Locate every blood parasite and identify its species.
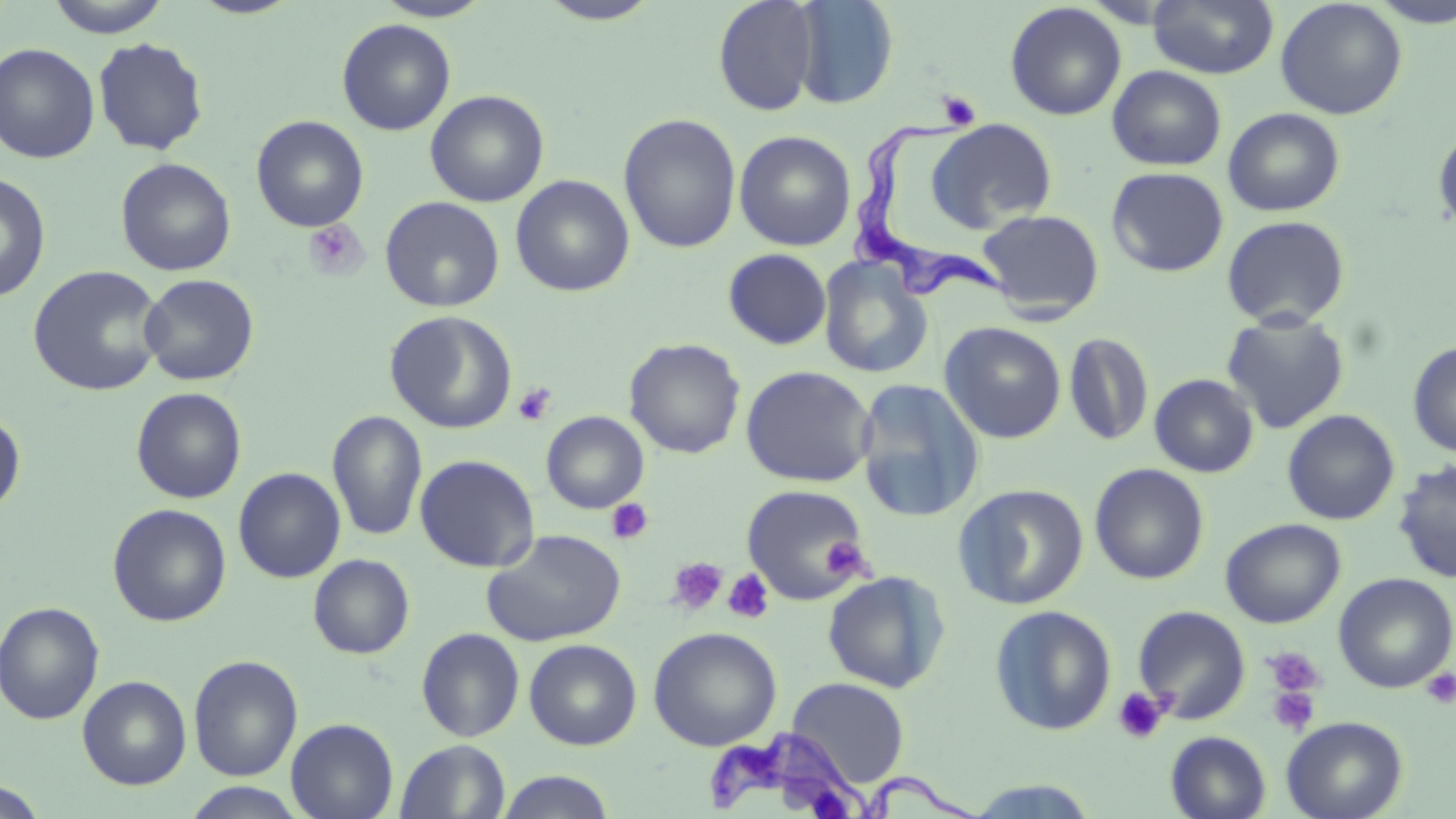
Approximate bounding boxes as [x1, y1, x2, y2] in pixels.
Trypanosoma brucei: [854, 116, 1014, 306], [707, 726, 970, 818].
No Plasmodium falciparum, Plasmodium ovale, Plasmodium malariae, Plasmodium vivax, or Babesia divergens observed.

Summary:
  - Uninfected red blood cell locations: [45, 0, 171, 37], [188, 0, 304, 19], [374, 0, 494, 21], [535, 0, 664, 25], [712, 0, 821, 115], [792, 0, 898, 110], [1147, 0, 1279, 79], [1275, 0, 1408, 120], [1368, 0, 1456, 28], [1005, 2, 1127, 121], [337, 18, 456, 135], [93, 37, 209, 156], [0, 42, 100, 163], [1107, 65, 1226, 171], [425, 90, 549, 207], [1223, 107, 1346, 216], [618, 113, 742, 253], [251, 115, 370, 232], [927, 118, 1057, 233], [1433, 126, 1456, 235], [734, 130, 857, 251], [116, 157, 236, 276], [1107, 167, 1228, 277], [0, 171, 51, 303], [511, 175, 634, 297], [379, 196, 505, 312], [977, 209, 1105, 319], [1222, 215, 1350, 328], [722, 248, 831, 350], [818, 255, 934, 379], [28, 264, 166, 397], [138, 273, 259, 386], [385, 310, 517, 433], [1220, 311, 1350, 434], [940, 321, 1067, 444], [1063, 332, 1154, 447], [624, 338, 746, 459], [1407, 341, 1456, 457], [740, 365, 876, 488], [1149, 373, 1259, 477], [854, 377, 985, 523], [131, 387, 246, 504], [0, 409, 26, 521], [1282, 409, 1400, 525], [327, 410, 427, 542], [541, 411, 649, 513], [415, 454, 540, 572], [1392, 460, 1456, 584], [1089, 463, 1210, 585], [233, 467, 346, 583], [740, 484, 872, 604], [952, 484, 1089, 610], [107, 503, 232, 627], [1220, 518, 1345, 628], [482, 529, 627, 647], [308, 554, 415, 659], [822, 571, 951, 693], [1334, 573, 1456, 693], [0, 601, 104, 725], [989, 605, 1117, 736], [1132, 605, 1251, 724], [648, 626, 782, 751], [416, 627, 525, 742], [524, 638, 642, 750], [188, 655, 303, 782], [77, 675, 192, 790], [787, 677, 910, 786], [1281, 716, 1408, 819], [286, 718, 398, 819], [1166, 731, 1271, 819], [395, 739, 511, 818], [496, 770, 617, 819], [0, 779, 48, 818], [958, 779, 1105, 818], [180, 782, 311, 819]
  - Platelet locations: [937, 90, 981, 130], [303, 219, 369, 281], [514, 383, 556, 426], [605, 498, 654, 546], [821, 537, 869, 577], [667, 556, 728, 615], [722, 569, 775, 625], [1262, 646, 1327, 701], [1420, 667, 1456, 709], [1266, 684, 1321, 736], [1112, 687, 1168, 745]
  - Slide-level diagnosis: Trypanosoma brucei
  - Image size: 1456×819 pixels
  - Field of view: single
  - Magnification: 1000x
  - Stain: May-Grünwald-Giemsa
  - Modality: light microscopy
  - Preparation: thin blood smear